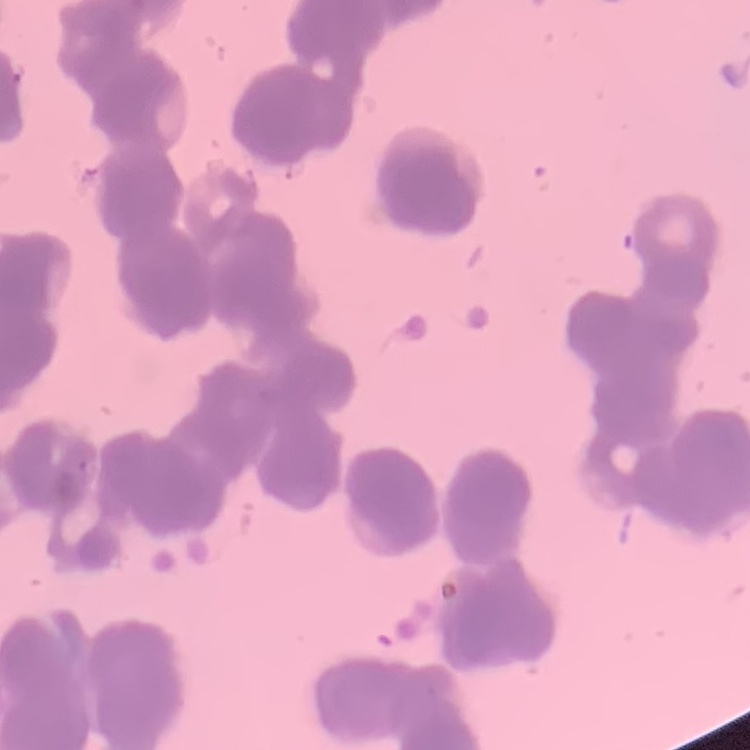
Summary:
  - Red blood cell morphology: rouleaux formation
  - Stain: Field's or Giemsa
  - Image type: square crop of a larger photomicrograph
  - Preparation: thin peripheral smear